Name the parasite shown.
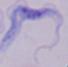

This is a trypanosome.

modality = photomicrograph
magnification = 1000x